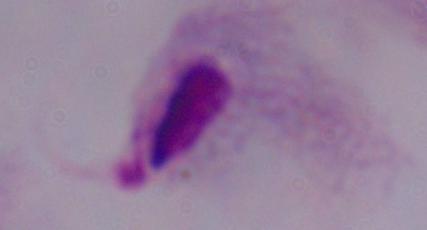 1000x magnification. A trichomonad is shown. Photomicrograph.